Name the cell type shown.
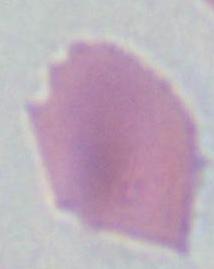

An erythrocyte.

Micrograph. 1000x magnification.